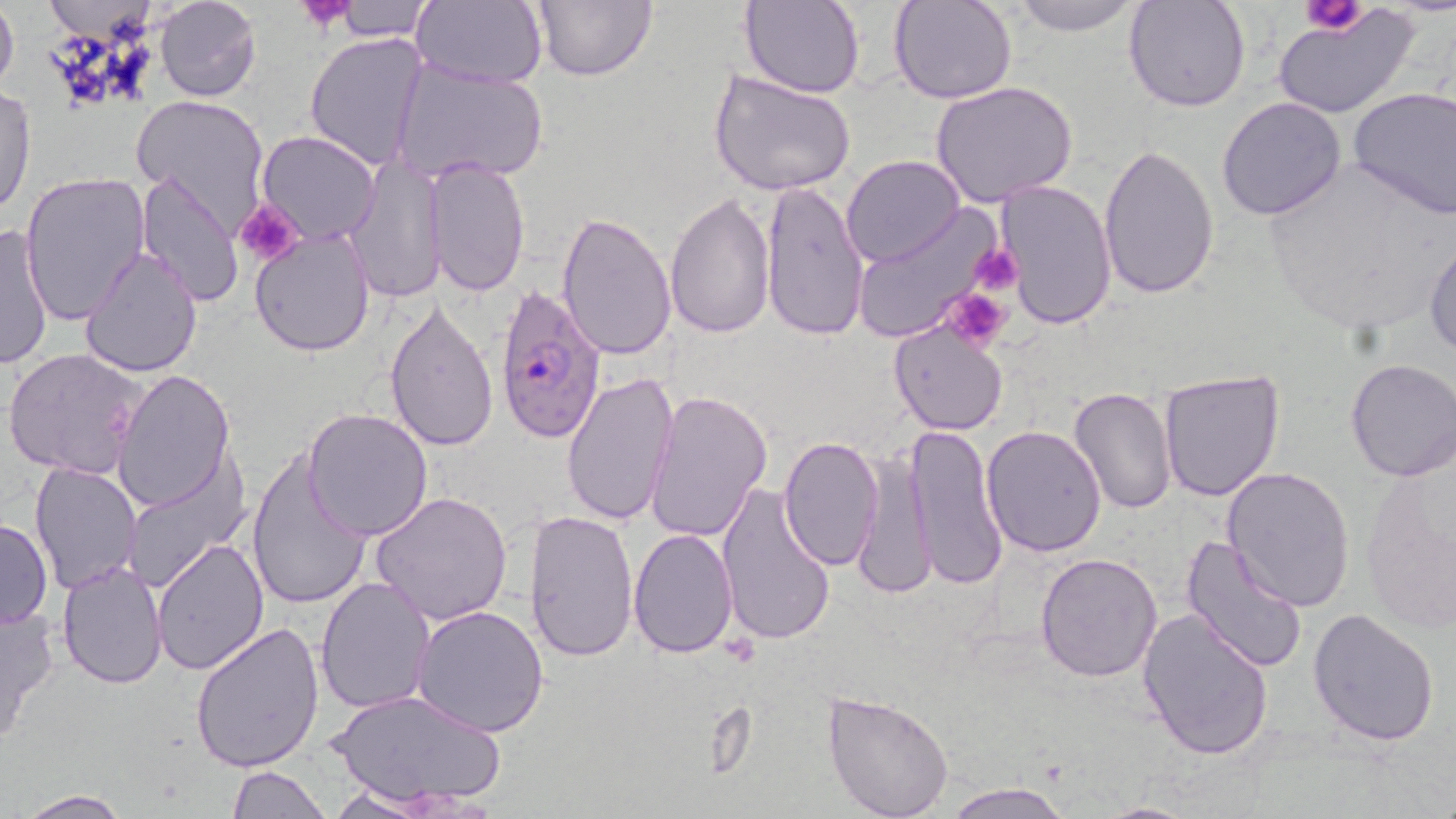

Approximate bounding boxes as (x1, y1, x2, y2) in pixels. Platelet locations: (298, 0, 353, 32), (1301, 0, 1366, 34), (235, 197, 306, 270), (969, 243, 1025, 296), (938, 289, 1014, 351). Plasmodium falciparum-infected red blood cell locations: (495, 285, 610, 444). Uninfected red blood cell locations: (0, 0, 19, 101), (151, 0, 262, 102), (327, 0, 438, 41), (413, 0, 548, 89), (530, 0, 656, 83), (740, 0, 865, 98), (892, 0, 1018, 104), (1004, 0, 1149, 35), (1124, 0, 1252, 111), (1273, 8, 1418, 121), (304, 33, 430, 173), (390, 57, 549, 188), (709, 67, 857, 197), (931, 82, 1078, 207), (0, 85, 36, 218), (1346, 87, 1456, 219), (131, 94, 270, 227), (1216, 97, 1347, 222), (257, 131, 381, 245), (1096, 143, 1220, 298), (427, 155, 529, 297), (345, 156, 445, 303), (842, 156, 965, 269), (1258, 164, 1450, 340), (135, 172, 242, 309), (21, 173, 150, 326), (993, 179, 1118, 334), (760, 180, 869, 343), (665, 193, 775, 341), (850, 209, 1003, 344), (556, 211, 678, 361), (0, 221, 55, 370), (250, 226, 376, 356), (1425, 240, 1456, 360), (79, 248, 203, 378), (383, 299, 500, 453), (889, 320, 1008, 436), (2, 347, 148, 481), (1343, 359, 1456, 482), (1159, 367, 1288, 503), (113, 370, 236, 514), (560, 370, 680, 528), (1068, 388, 1179, 516), (645, 389, 773, 542), (302, 408, 434, 541), (982, 425, 1109, 558), (904, 426, 1009, 592), (778, 437, 885, 572), (852, 447, 936, 602), (247, 449, 372, 612), (29, 463, 143, 594), (122, 463, 250, 594), (1222, 467, 1355, 613), (717, 480, 837, 647), (371, 492, 514, 627), (523, 509, 638, 663), (0, 518, 52, 631), (628, 529, 740, 659), (1180, 535, 1307, 674), (152, 536, 270, 674), (1036, 552, 1165, 683), (58, 558, 169, 687), (315, 575, 435, 713), (0, 600, 56, 749), (411, 603, 551, 738), (1308, 608, 1440, 745), (1138, 609, 1274, 761), (190, 620, 325, 772), (330, 686, 505, 813), (821, 689, 954, 819), (225, 764, 328, 819), (940, 781, 1074, 819), (320, 786, 446, 819), (15, 791, 130, 819), (1087, 800, 1199, 819). Slide-level diagnosis: Plasmodium falciparum. Light microscopy. One field of a larger specimen. May-Grünwald-Giemsa stain. Image is 1456×819 pixels. 1000x magnification. Thin blood smear.